Comment on the morphology of the red blood cells.
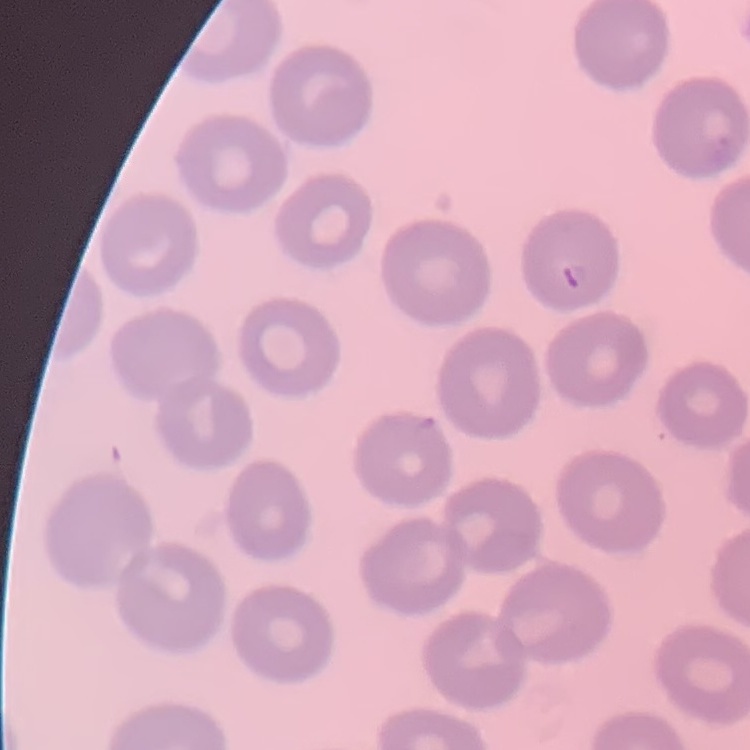

They show no rouleaux formation.

image type = square crop of a larger photomicrograph
stain = Field's or Giemsa
preparation = thin peripheral smear